Classify this cell by malaria status.
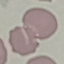
It is uninfected.

preparation = thin blood smear
image type = automatically extracted cell patch, resized to 64 × 64 pixels
stain = Giemsa
capture = smartphone camera at the microscope eyepiece